State which cell type is depicted.
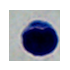
A leukocyte.

magnification = 1000x
modality = micrograph